State the blood parasite species.
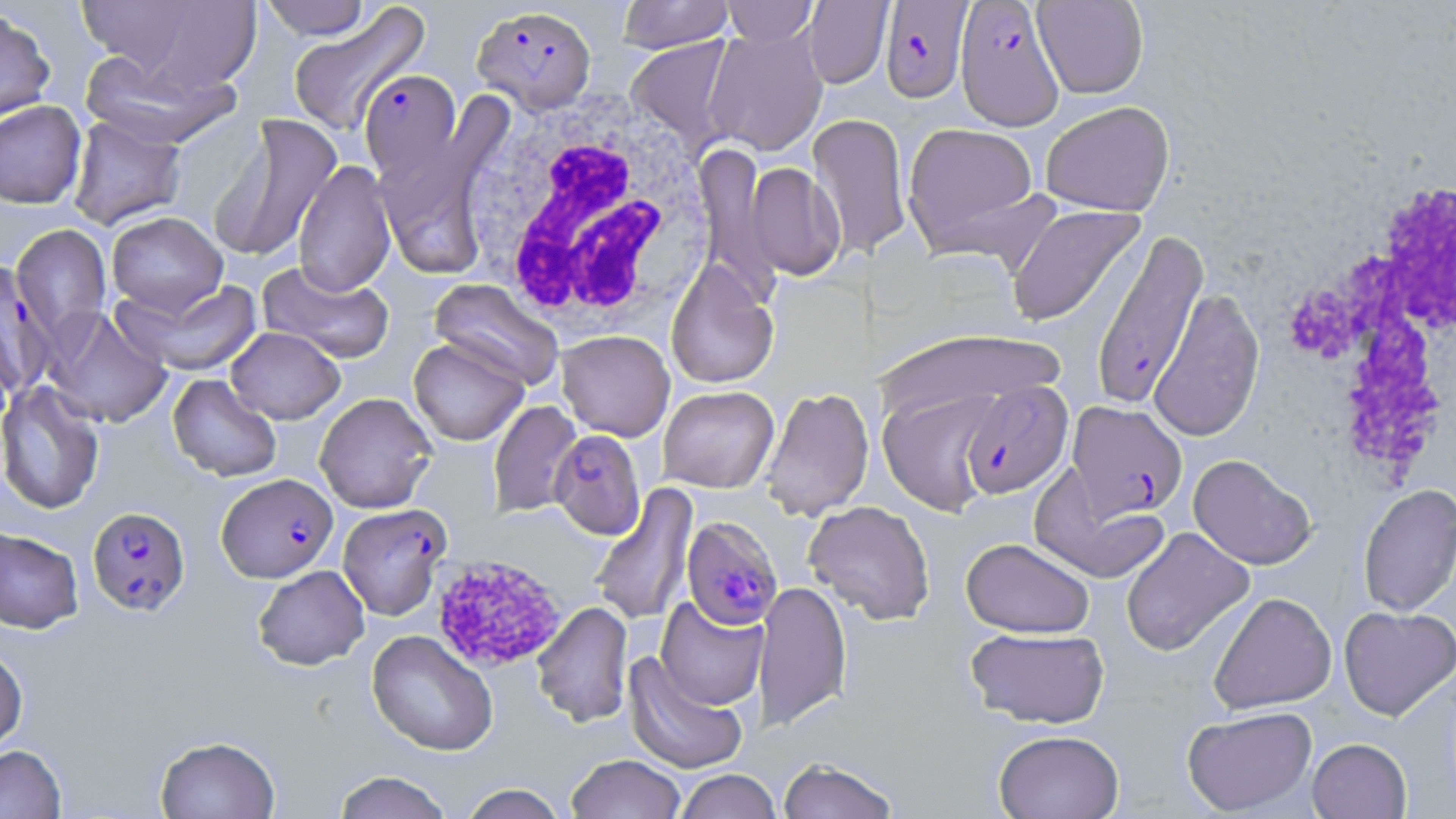
Plasmodium falciparum.

Approximate bounding boxes as (x1,y1)-(x2,y2) corner pairs in pixels. White blood cell locations: (463,88)-(716,339), (1287,174)-(1456,494). Uninfected red blood cell locations: (77,0)-(262,97), (258,0)-(373,40), (617,0)-(734,53), (722,1)-(819,47), (802,1)-(893,88), (1032,1)-(1149,99), (286,4)-(430,136), (0,5)-(56,126), (703,27)-(828,156), (625,36)-(738,154), (79,49)-(239,147), (0,100)-(87,209), (1040,101)-(1175,216), (808,112)-(911,258), (374,113)-(504,280), (67,114)-(187,230), (209,116)-(342,263), (902,122)-(1041,255), (694,144)-(778,300), (293,158)-(396,297), (744,161)-(845,281), (1005,204)-(1146,329), (106,211)-(228,318), (11,223)-(112,344), (665,260)-(779,389), (257,261)-(395,365), (118,276)-(265,376), (429,279)-(564,392), (1148,286)-(1265,442), (42,305)-(173,429), (225,326)-(345,424), (874,326)-(1064,426), (557,330)-(675,441), (408,337)-(528,446), (168,374)-(283,482), (0,381)-(105,515), (658,386)-(779,492), (760,386)-(874,521), (877,386)-(1003,516), (314,392)-(437,513), (488,400)-(583,518), (1188,454)-(1317,571), (1029,466)-(1169,585), (589,483)-(699,628), (1357,483)-(1456,617), (804,500)-(935,625), (0,526)-(83,634), (1120,526)-(1255,657), (961,537)-(1095,638), (253,565)-(370,671), (753,579)-(852,732), (1207,591)-(1337,715), (655,596)-(768,711), (532,602)-(632,727), (1339,605)-(1456,721), (964,626)-(1110,729), (367,630)-(498,756), (0,645)-(28,752), (623,652)-(748,775), (1181,706)-(1318,816), (993,730)-(1124,819), (155,735)-(280,819), (1307,738)-(1412,818), (0,744)-(66,819), (565,754)-(686,819), (777,758)-(900,819), (674,769)-(781,819), (332,771)-(454,819), (458,783)-(567,819). Plasmodium falciparum-infected red blood cell locations: (880,1)-(973,103), (955,1)-(1064,131), (471,4)-(597,114), (359,69)-(462,183), (1090,229)-(1208,411), (1,260)-(54,397), (960,379)-(1073,499), (1067,401)-(1188,520), (549,429)-(645,539), (216,473)-(337,582), (337,502)-(451,621), (87,506)-(190,615), (681,516)-(783,631). Platelet locations: (429,553)-(568,673). 1000x magnification. Image is 1456×819 pixels. One field of a larger specimen. Light microscopy. May-Grünwald-Giemsa stain. Thin blood film.